Assess the morphology of the red blood cells.
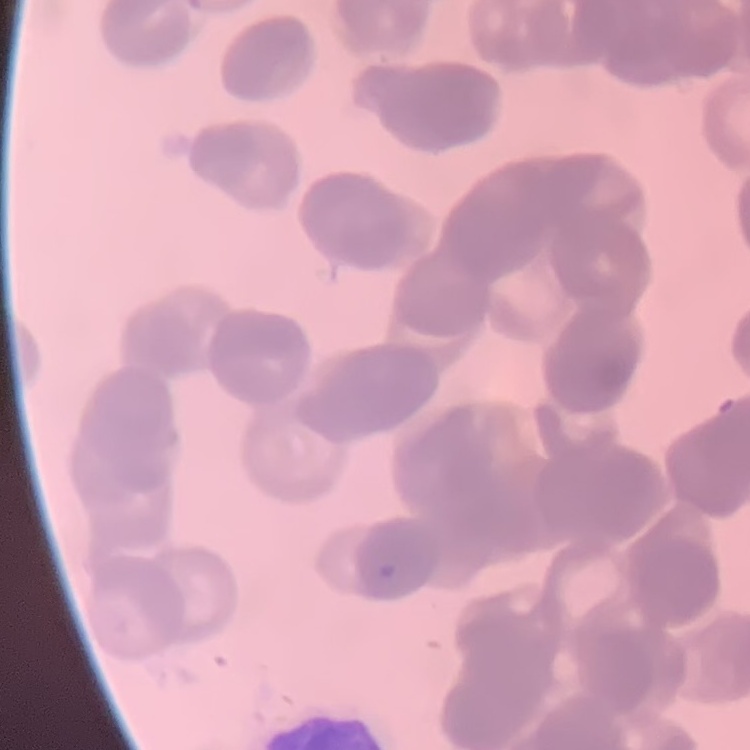
They show rouleaux formation.

Stained with either Field's or Giemsa. Thin peripheral smear. One tile cut from a larger photomicrograph.